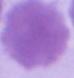
modality = micrograph
identification = red blood cell
magnification = 1000x